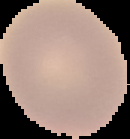
Summary:
  - Preparation: thin blood film
  - Image type: cell region segmented out of the field of view; surrounding area masked to black
  - Malaria status: uninfected
  - Image size: 130×139 pixels